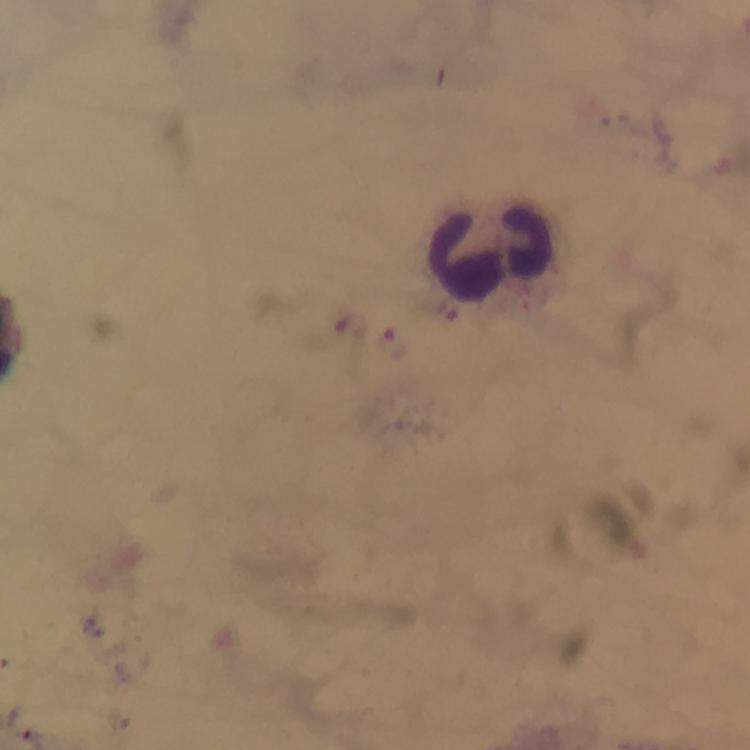

Approximate centers as (x, y) in pixels.
Summary:
  - Leukocyte locations: (490, 253)
  - Plasmodium parasite locations: (349, 327), (396, 343)
  - Immersion oil: used
  - Magnification: 100x
  - Cropped from: a single field of view
  - Image size: 750×750 pixels
  - Preparation: thick smear
  - Capture: smartphone mounted on the microscope
  - Stain: Giemsa
  - Context: from a diagnostic examination for malaria